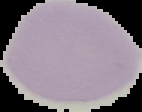
From a thin blood film. Image is 142×112 pixels. Malaria status: uninfected. The area outside the segmented cell region is set to black.